Assess for malaria.
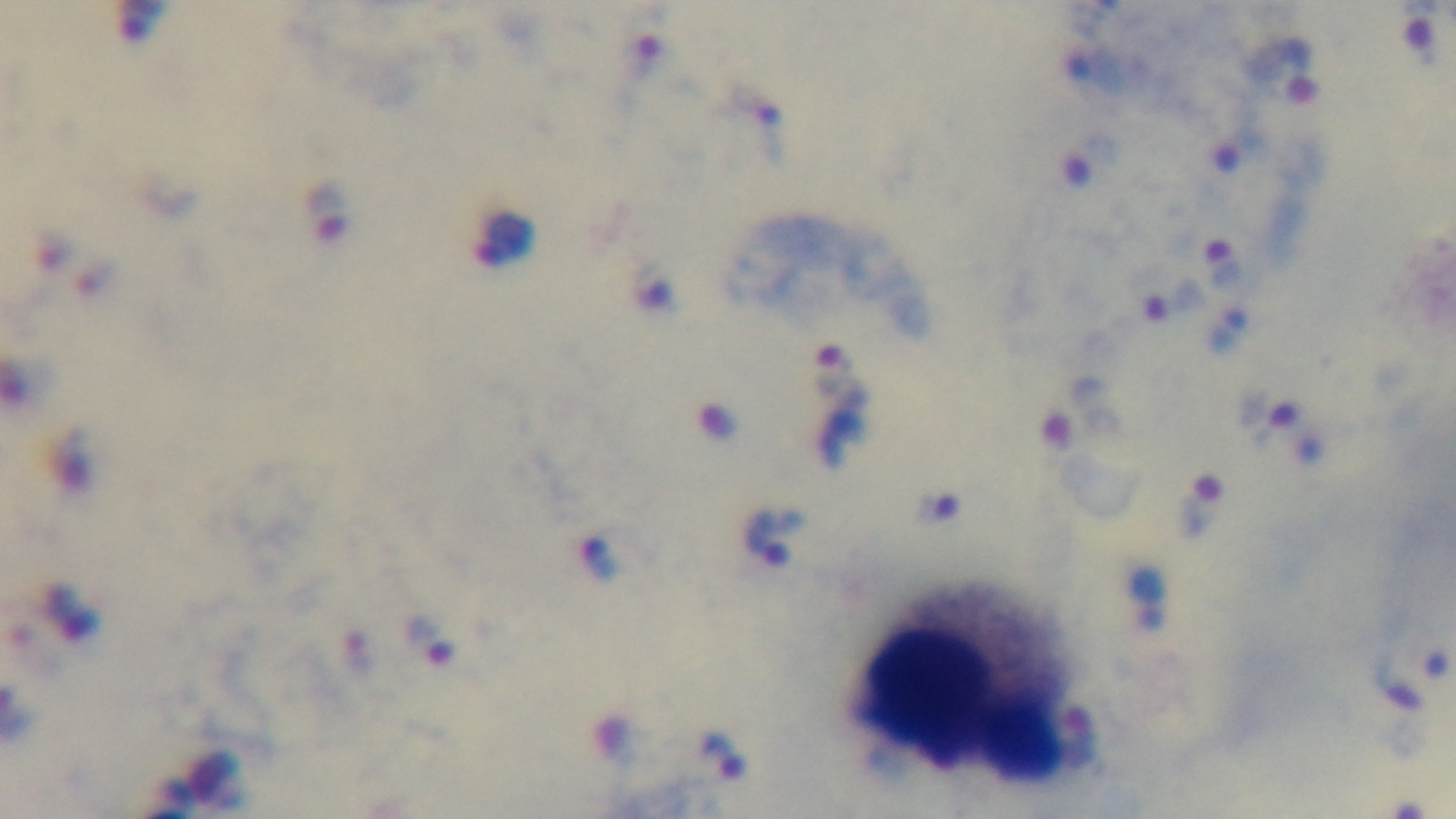

Infected.

Giemsa stain. Preparation: thick. Light microscopy. Mounted 4K digital camera. Single field of view. 100x oil-immersion objective.